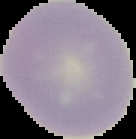
Image is 136×139 pixels. Malaria status: uninfected. From a thin blood smear. Cell region segmented out of the field of view; the surrounding area is masked to black.